Locate every blood parasite and identify its species.
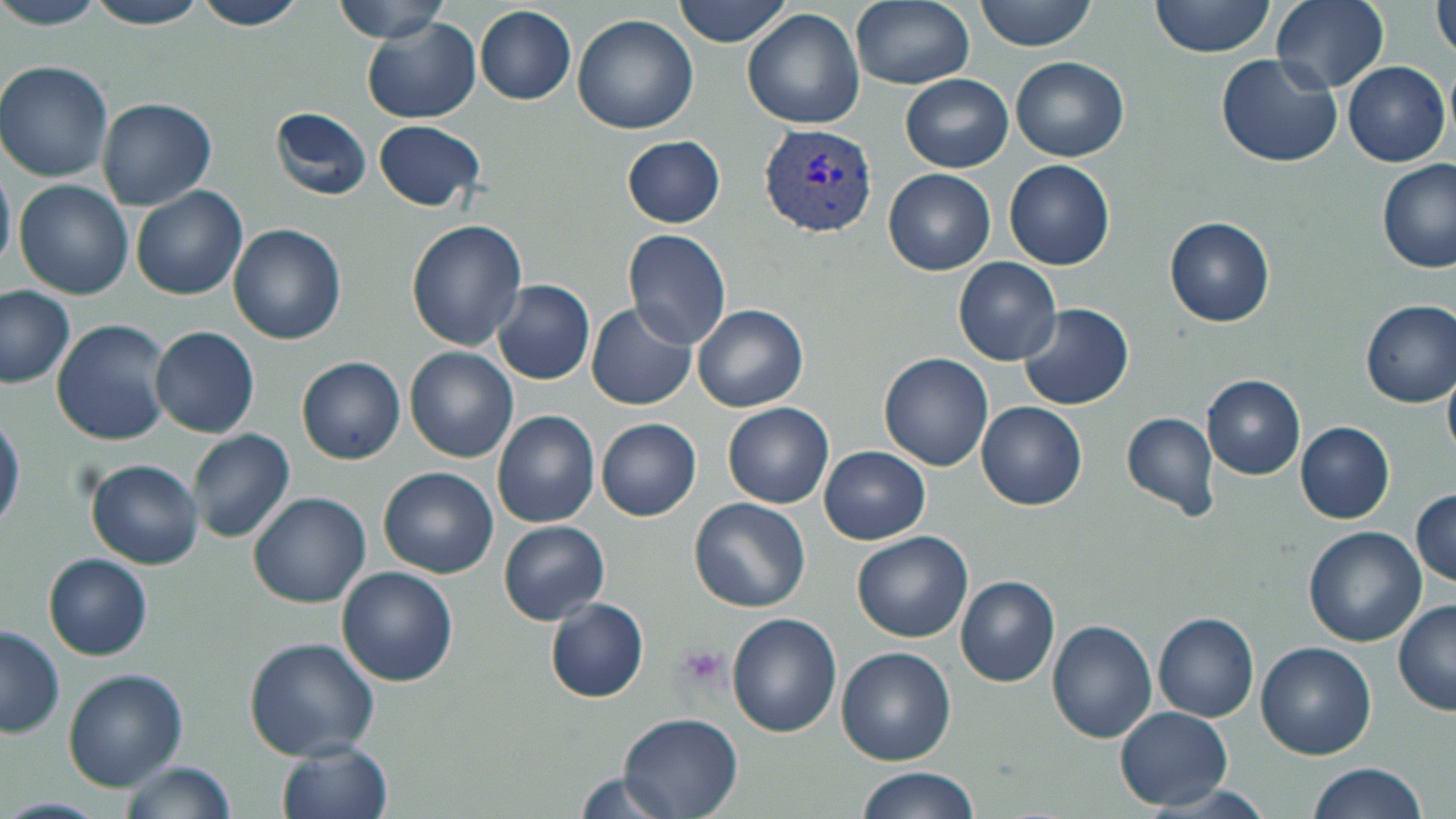
Approximate bounding boxes as [x1, y1, x2, y2] in pixels.
Plasmodium vivax-infected red blood cells: [759, 122, 881, 237].
No Plasmodium falciparum, Plasmodium ovale, Plasmodium malariae, Babesia divergens, or Trypanosoma brucei observed.

Summary:
  - Platelet locations: [674, 644, 731, 694]
  - Uninfected red blood cell locations: [79, 0, 213, 29], [331, 0, 454, 44], [675, 0, 795, 47], [850, 0, 974, 89], [976, 0, 1096, 52], [1149, 0, 1276, 57], [1271, 0, 1390, 91], [1433, 0, 1456, 62], [191, 1, 307, 31], [0, 2, 107, 31], [474, 5, 577, 104], [743, 9, 866, 130], [571, 13, 698, 135], [363, 18, 479, 122], [1216, 52, 1342, 167], [1010, 55, 1129, 162], [0, 60, 114, 181], [1342, 62, 1450, 166], [901, 75, 1013, 172], [95, 98, 216, 209], [272, 108, 372, 200], [374, 121, 485, 209], [621, 135, 726, 228], [1005, 160, 1116, 270], [1378, 160, 1455, 273], [0, 162, 15, 272], [884, 168, 995, 274], [15, 180, 133, 300], [132, 185, 247, 300], [1165, 215, 1276, 327], [407, 221, 528, 350], [228, 224, 347, 344], [623, 227, 732, 350], [953, 257, 1062, 365], [492, 280, 595, 386], [0, 286, 75, 388], [1361, 300, 1456, 406], [587, 303, 696, 410], [1020, 303, 1133, 411], [694, 304, 808, 413], [53, 319, 173, 445], [152, 327, 259, 437], [406, 348, 518, 462], [880, 352, 993, 472], [298, 357, 406, 465], [1444, 371, 1456, 461], [1202, 374, 1305, 479], [723, 401, 834, 509], [976, 401, 1086, 508], [0, 406, 23, 535], [493, 410, 600, 528], [1121, 411, 1220, 520], [597, 418, 701, 521], [1295, 420, 1396, 523], [188, 428, 295, 544], [92, 440, 300, 553], [819, 445, 930, 545], [86, 459, 203, 569], [379, 467, 499, 579], [1412, 489, 1455, 588], [249, 493, 371, 608], [689, 497, 811, 612], [498, 521, 610, 624], [1303, 527, 1427, 648], [852, 531, 972, 642], [44, 553, 151, 660], [337, 566, 457, 686], [956, 576, 1059, 687], [546, 598, 649, 702], [1395, 599, 1455, 715], [1154, 612, 1260, 723], [728, 613, 843, 737], [1047, 619, 1155, 743], [0, 624, 64, 738], [245, 638, 381, 760], [1256, 642, 1376, 760], [837, 647, 957, 765], [63, 670, 185, 791], [1115, 707, 1234, 812], [619, 714, 741, 816], [276, 739, 392, 819], [115, 760, 235, 819], [1303, 763, 1427, 819], [854, 768, 982, 819], [574, 770, 686, 818]
  - Slide-level diagnosis: Plasmodium vivax
  - Modality: optical microscopy
  - Magnification: 1000x
  - Field of view: one of a larger specimen
  - Stain: May-Grünwald-Giemsa
  - Image size: 1456×819 pixels
  - Preparation: thin blood film